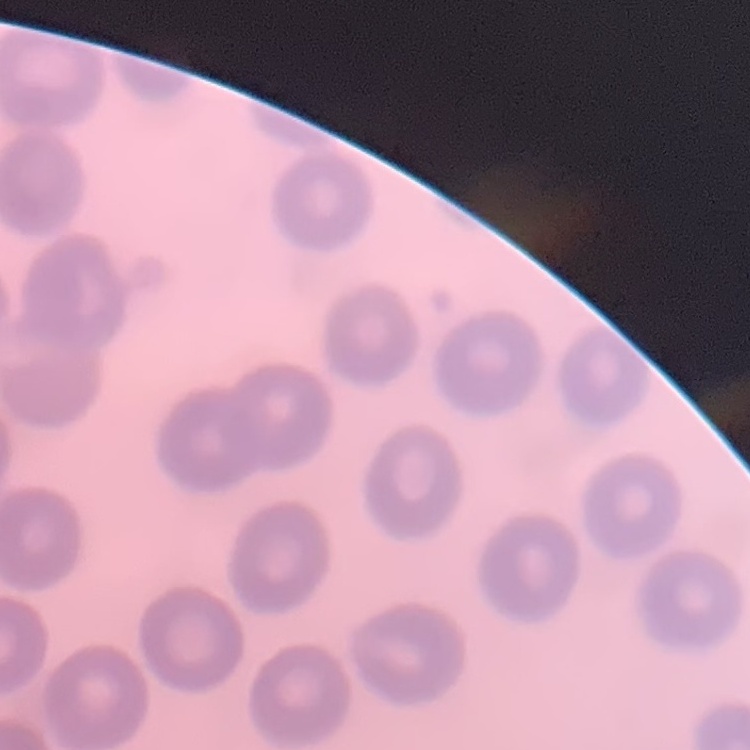

{
  "red_blood_cell_morphology": "no rouleaux formation",
  "preparation": "thin blood film",
  "image_type": "square crop of a larger photomicrograph",
  "stain": "Field's or Giemsa"
}